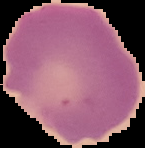 The area outside the segmented cell region is set to black. Image is 145×148 pixels. Result: negative for malaria parasites. From a thin blood film.